Assess this cell for malaria.
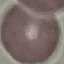

Uninfected.

Thin blood film. Photographed with a smartphone camera at the microscope eyepiece. Cell patch, automatically extracted from a larger field of view and resized to 64 × 64 pixels. Giemsa-stained preparation.